Report the malaria status of this cell.
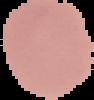

Uninfected.

preparation = thin blood film
image size = 94×100 pixels
image type = segmented cell region with the area outside set to black